Comment on the morphology of the red blood cells.
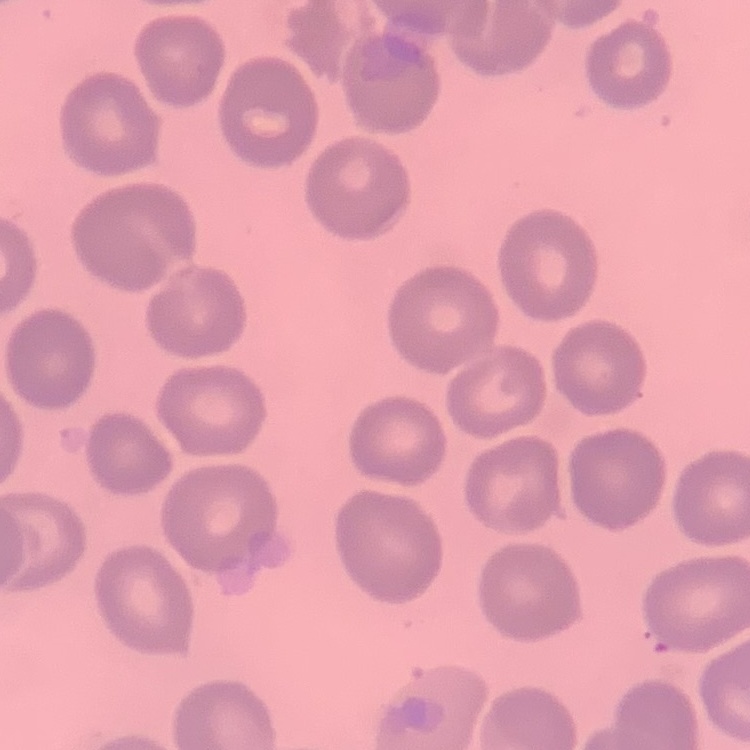
They show no rouleaux formation.

Stained with either Field's or Giemsa. Thin blood film. Square crop of a larger photomicrograph.